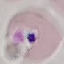
Summary:
  - Result: negative for malaria parasites
  - Preparation: thin blood film
  - Image type: cell patch, automatically extracted from a larger field of view and resized to 64 × 64 pixels
  - Stain: Giemsa
  - Capture: smartphone through the microscope eyepiece